State which cell type is depicted.
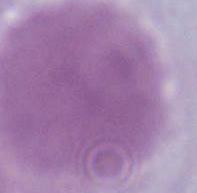
An erythrocyte.

Micrograph. Captured at 1000x magnification.